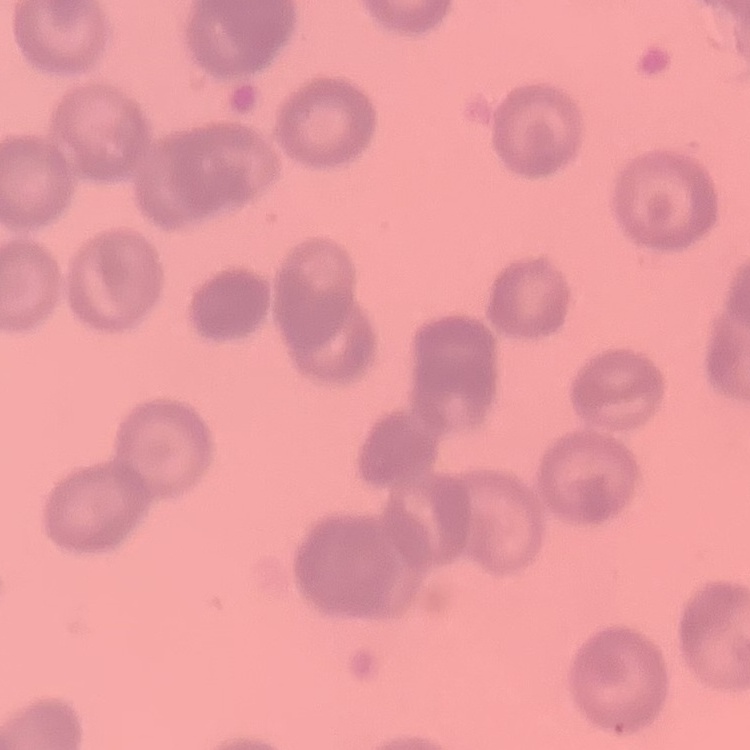

erythrocyte morphology = rouleaux formation
image type = square crop of a larger photomicrograph
stain = Field's or Giemsa
preparation = thin blood smear